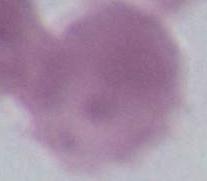

Photomicrograph. Captured at 1000x magnification. A red blood cell is shown.